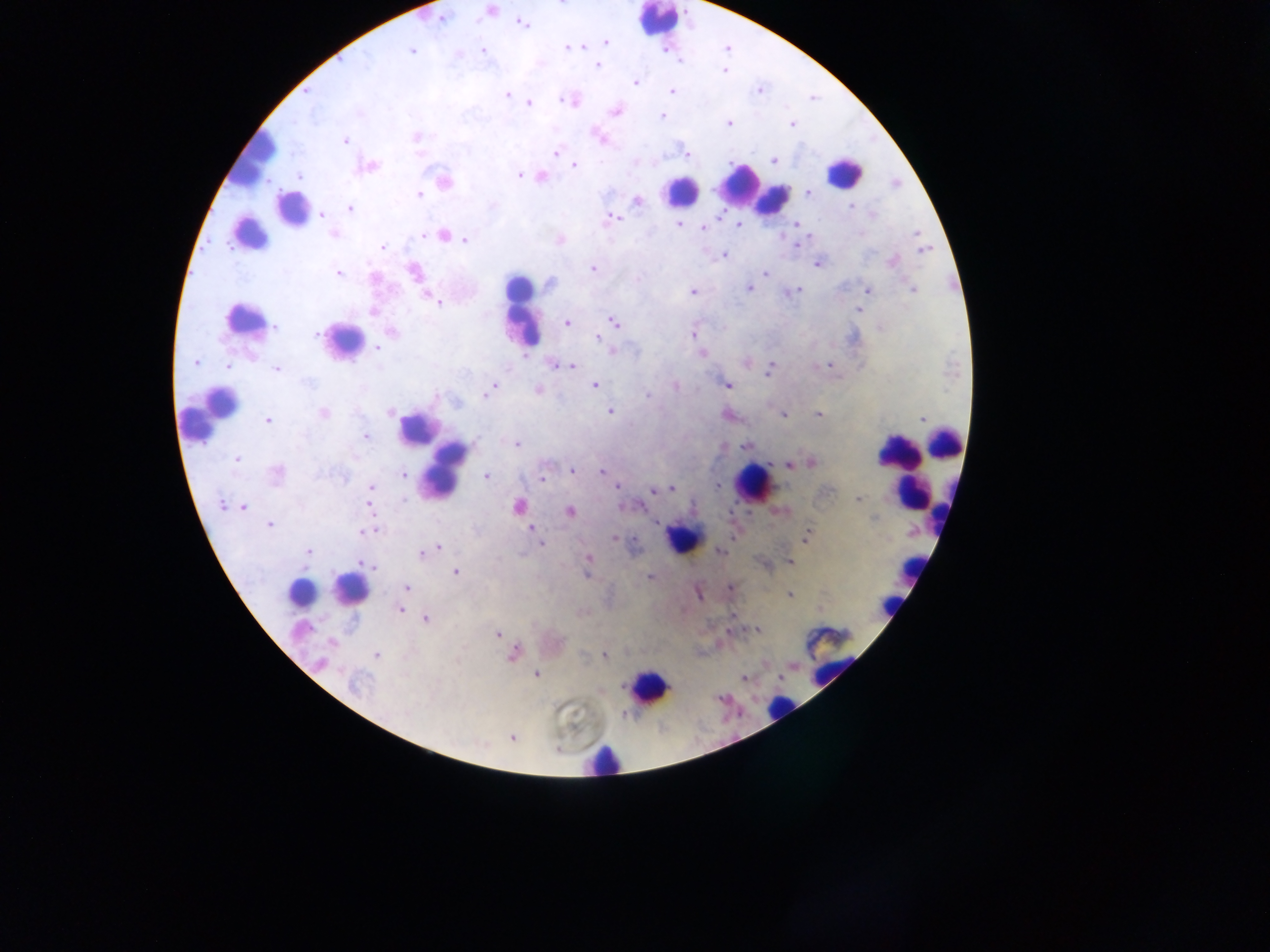 Approximate centers as x y in pixels. Plasmodium parasite locations: 491 10; 442 19; 522 23; 606 41; 568 47; 483 50; 411 51; 597 65; 724 70; 635 82; 759 91; 670 92; 506 95; 565 100; 529 103; 615 111; 359 112; 662 116; 728 124; 792 124; 416 136; 599 138; 345 141; 556 153; 685 153; 774 160; 368 166; 574 166; 519 174; 299 176; 541 177; 445 181; 807 193; 419 194; 638 201; 850 207; 350 208; 322 215; 872 215; 611 218; 678 224; 738 224; 797 224; 703 228; 916 233; 333 235; 424 236; 443 236; 465 240; 560 240; 797 245; 383 247; 924 250; 724 254; 892 261; 817 264; 593 269; 414 272; 765 272; 338 273; 375 280; 550 283; 748 288; 912 289; 869 290; 693 291; 794 292; 429 298; 437 302; 858 310; 373 311; 613 322; 567 323; 275 327; 392 332; 316 335; 693 335; 598 338; 378 348; 702 354; 195 363; 228 365; 554 365; 829 365; 571 366; 276 368; 770 369; 308 382; 728 385; 594 386; 675 386; 490 390; 537 390; 647 396; 436 397; 610 411; 390 412; 323 413; 818 414; 783 415; 921 419; 268 420; 366 436; 517 444; 745 446; 237 460; 812 463; 788 465; 572 470; 601 471; 276 474; 403 474; 486 476; 543 477; 717 485; 617 487; 370 488; 671 489; 656 490; 663 490; 404 499; 858 500; 221 505; 518 506; 243 507; 570 512; 873 518; 269 525; 371 529; 531 529; 366 532; 807 537; 614 539; 538 541; 542 544; 439 548; 432 550; 720 551; 308 552; 423 554; 588 560; 791 562; 367 564; 456 572; 587 573; 649 577; 407 588; 730 589; 791 594; 401 610; 426 619; 757 630; 498 634; 331 642; 512 654; 376 655; 604 655; 320 663; 536 674; 743 678; 354 683; 511 737. Leukocyte locations: 658 19; 252 159; 843 172; 740 183; 680 189; 771 198; 291 208; 522 310; 243 317; 344 339; 210 412; 417 428; 944 442; 896 452; 445 468; 752 484; 908 493; 682 537; 911 569; 352 588; 300 592; 830 664; 648 688; 779 709; 602 758. Object labeled both Plasmodium parasite and leukocyte by the source: 248 234. Thick blood smear. Image is 1270×952 pixels. Photographed through a microscope with a mobile-phone camera. One field of view. Collected in Ghana.